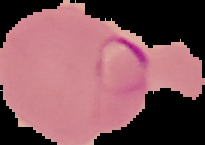
malaria status = parasitized
preparation = thin blood smear
image size = 205×145 pixels
image type = segmented cell region on a black background